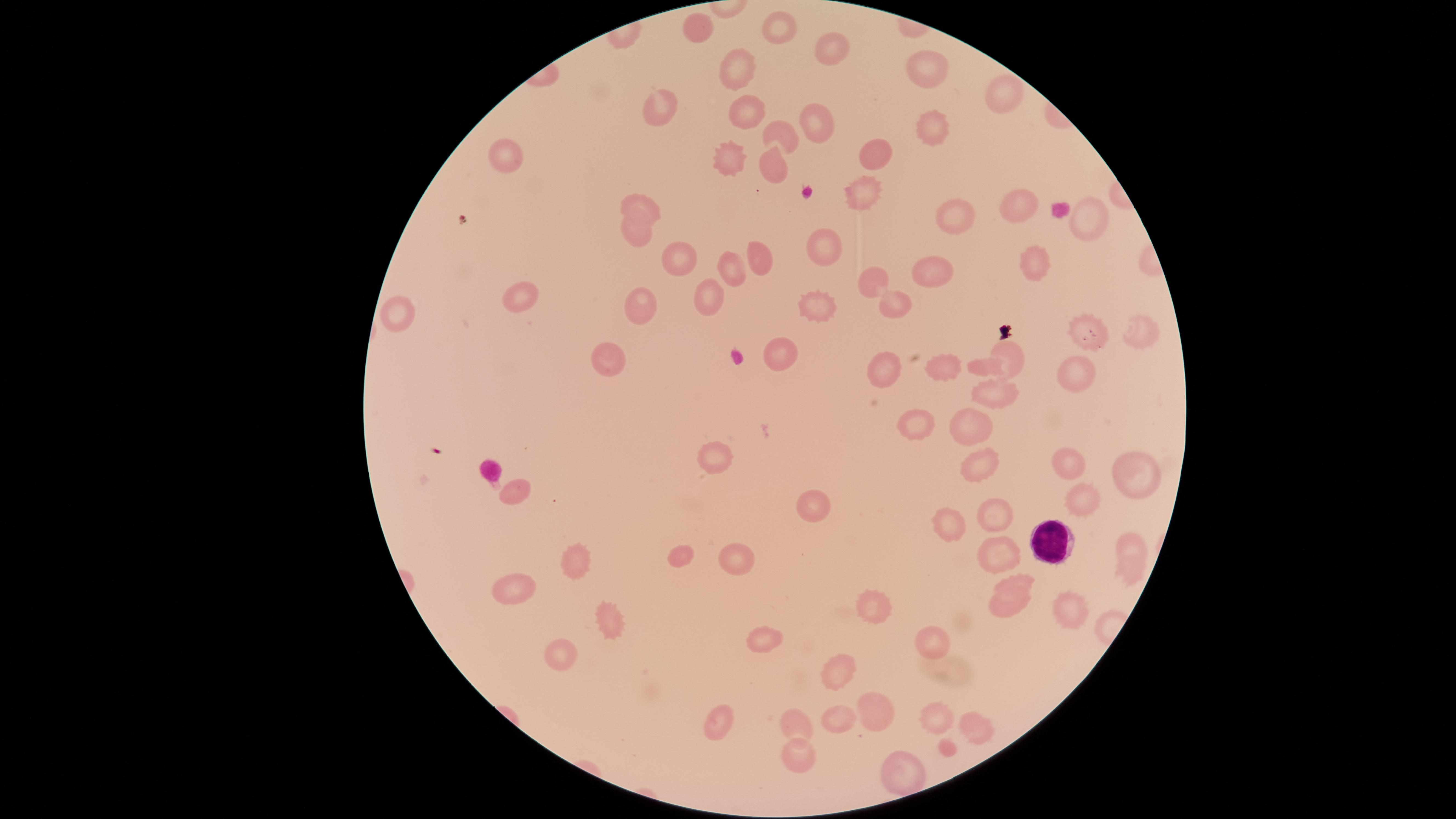 Approximate marker points as {x, y} in pixels. White blood cells: {1047, 540}. Uninfected red blood cells: {695, 28}, {780, 31}, {829, 49}, {743, 69}, {926, 70}, {1004, 95}, {743, 108}, {661, 114}, {815, 115}, {936, 124}, {785, 133}, {505, 155}, {872, 155}, {731, 157}, {774, 167}, {863, 197}, {641, 206}, {1016, 207}, {1089, 218}, {956, 219}, {636, 231}, {819, 249}, {678, 260}, {764, 260}, {1035, 266}, {730, 267}, {933, 272}, {870, 281}, {715, 294}, {889, 299}, {522, 303}, {812, 303}, {645, 307}, {399, 313}, {1138, 324}, {1077, 325}, {1008, 351}, {777, 354}, {610, 359}, {933, 363}, {885, 367}, {1076, 384}, {990, 394}, {920, 426}, {973, 431}, {712, 456}, {1076, 465}, {983, 467}, {1131, 477}, {513, 490}, {813, 502}, {1090, 502}, {997, 519}, {953, 531}, {1128, 540}, {686, 556}, {997, 560}, {737, 566}, {583, 569}, {1131, 576}, {1023, 583}, {514, 590}, {868, 602}, {1003, 606}, {617, 618}, {760, 640}, {931, 642}, {559, 652}, {837, 680}, {869, 705}, {935, 718}, {837, 719}, {796, 722}, {716, 723}, {976, 736}, {800, 756}, {909, 774}. Smartphone photograph through the microscope eyepiece. The visible region is circular. Presence: no malaria parasites detected. Thin blood film. Giemsa stain. Image is 1456×819 pixels. Single field of view.